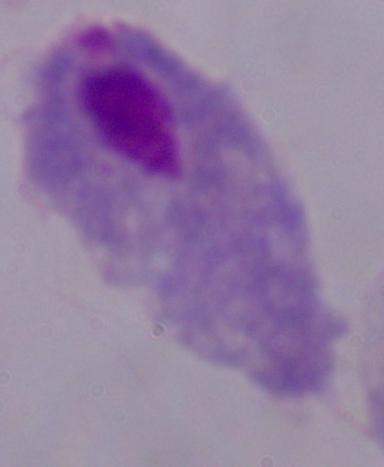

Captured at 1000x magnification. Photomicrograph. A trichomonad is shown.